Report the malaria status of this cell.
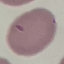

It is uninfected.

capture = smartphone through the microscope eyepiece
stain = Giemsa
preparation = thin blood smear
image type = cell patch, automatically extracted from a larger field of view and resized to 64 × 64 pixels